Classify this cell by malaria status.
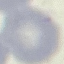

It is uninfected.

capture = smartphone camera at the microscope eyepiece
stain = Giemsa
image type = automatically extracted cell patch, resized to 64 × 64 pixels
preparation = thin smear